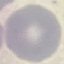
{
  "result": "no malaria parasites seen",
  "capture": "smartphone camera at the microscope eyepiece",
  "image_type": "cell patch, automatically extracted from a larger field of view and resized to 64 × 64 pixels",
  "preparation": "thin blood smear",
  "stain": "Giemsa"
}